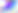
magnification = 400x
modality = photomicrograph
identification = Toxoplasma gondii